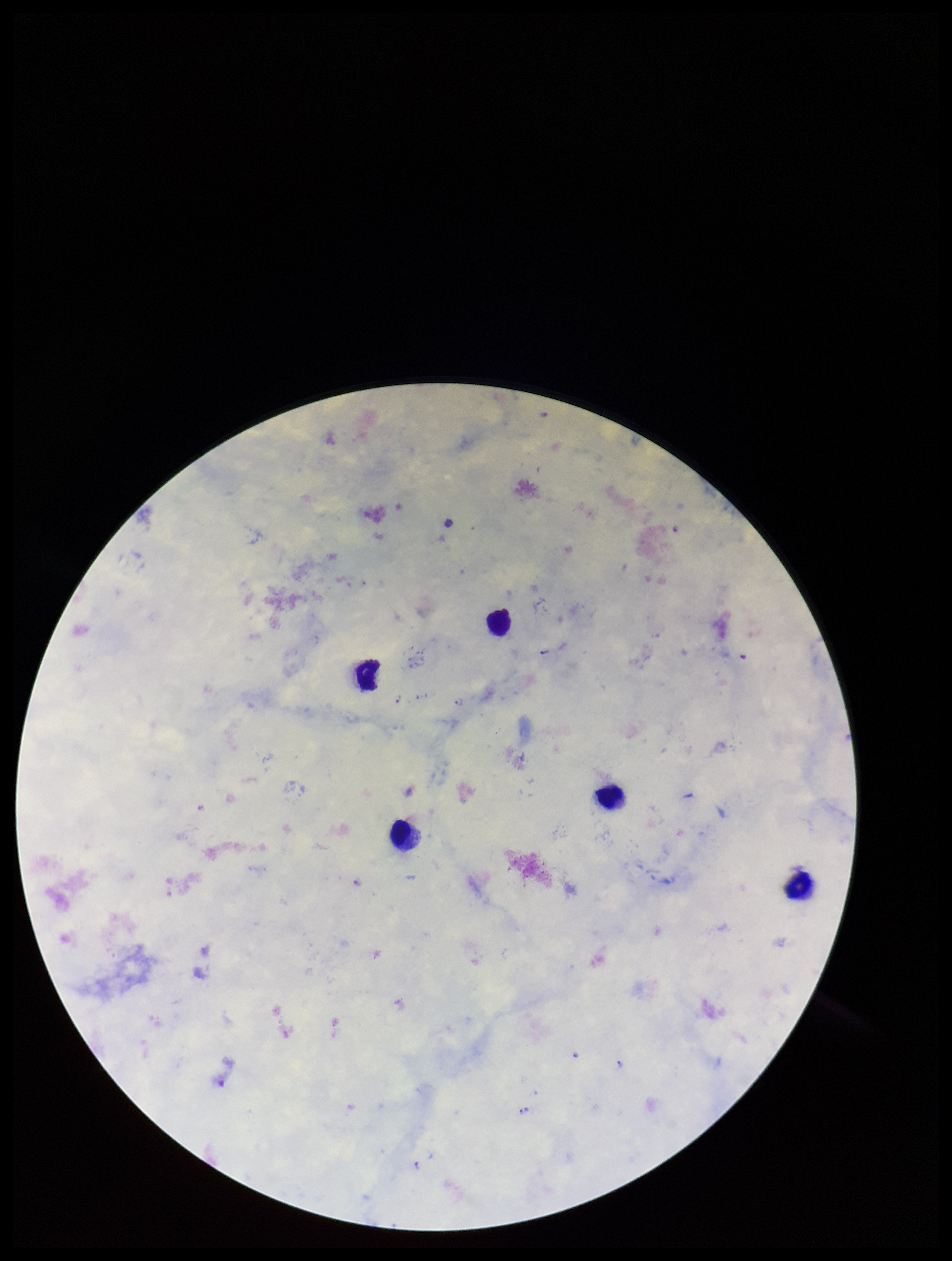
capture = smartphone photograph through the microscope eyepiece
stain = Giemsa
species reported for this patient = Plasmodium falciparum
image size = 952×1261 pixels
leukocyte count = 5
Plasmodium parasites = detected
patient malaria status = infected
preparation = thick blood smear
field of view = one from this slide
parasite count = 3